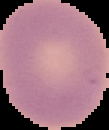
preparation: thin blood smear
result: no malaria parasites detected
image_type: cell region segmented out of the field of view; surrounding area masked to black
image_size: 109×130 pixels